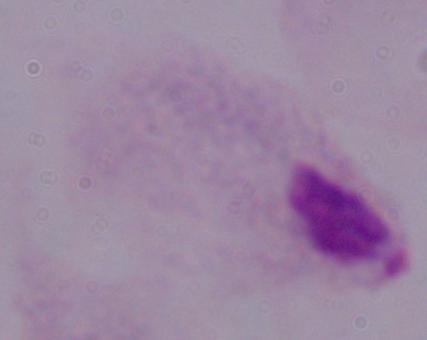

{
  "magnification": "1000x",
  "modality": "micrograph",
  "identification": "trichomonad"
}